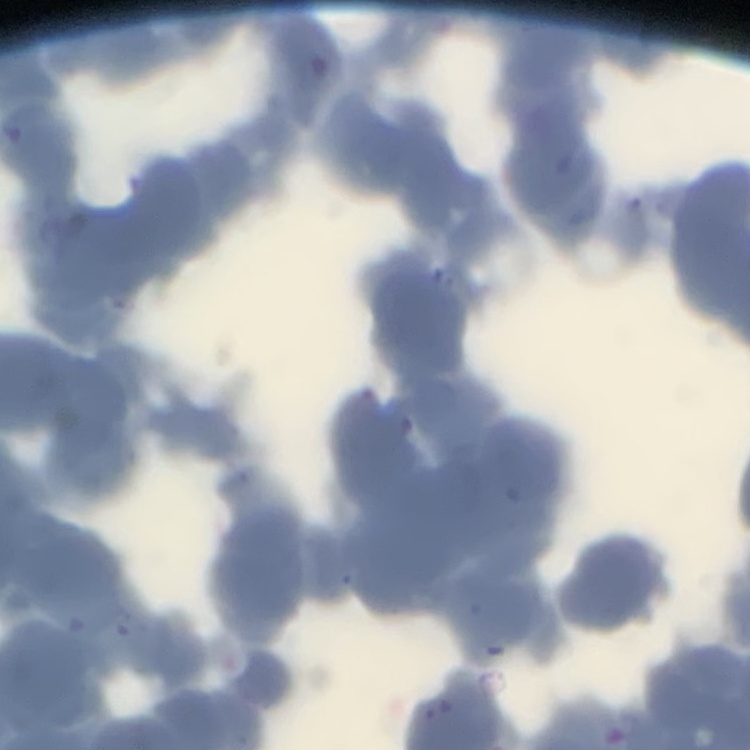
The red blood cells show rouleaux formation. Field's or Giemsa stain. One tile cut from a larger photomicrograph. Thin blood smear.